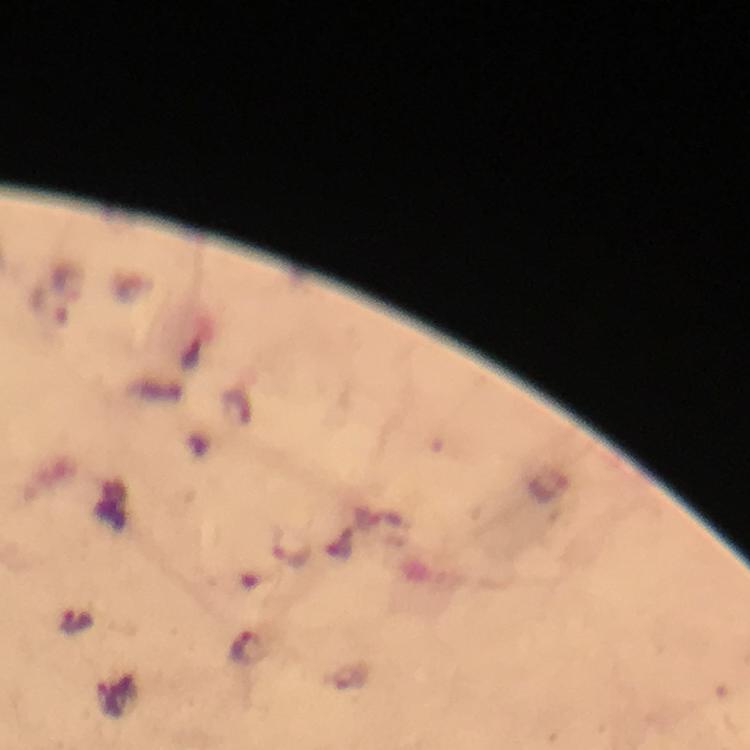
Approximate centers as {x, y} in pixels. Plasmodium parasite locations: {77, 622}, {247, 647}. Image is 750×750 pixels. A crop from one field of view. Immersion oil was used. Giemsa stain. At 100x magnification. From a malaria diagnostic workup. Thick smear. Photographed with a smartphone mounted on the microscope.